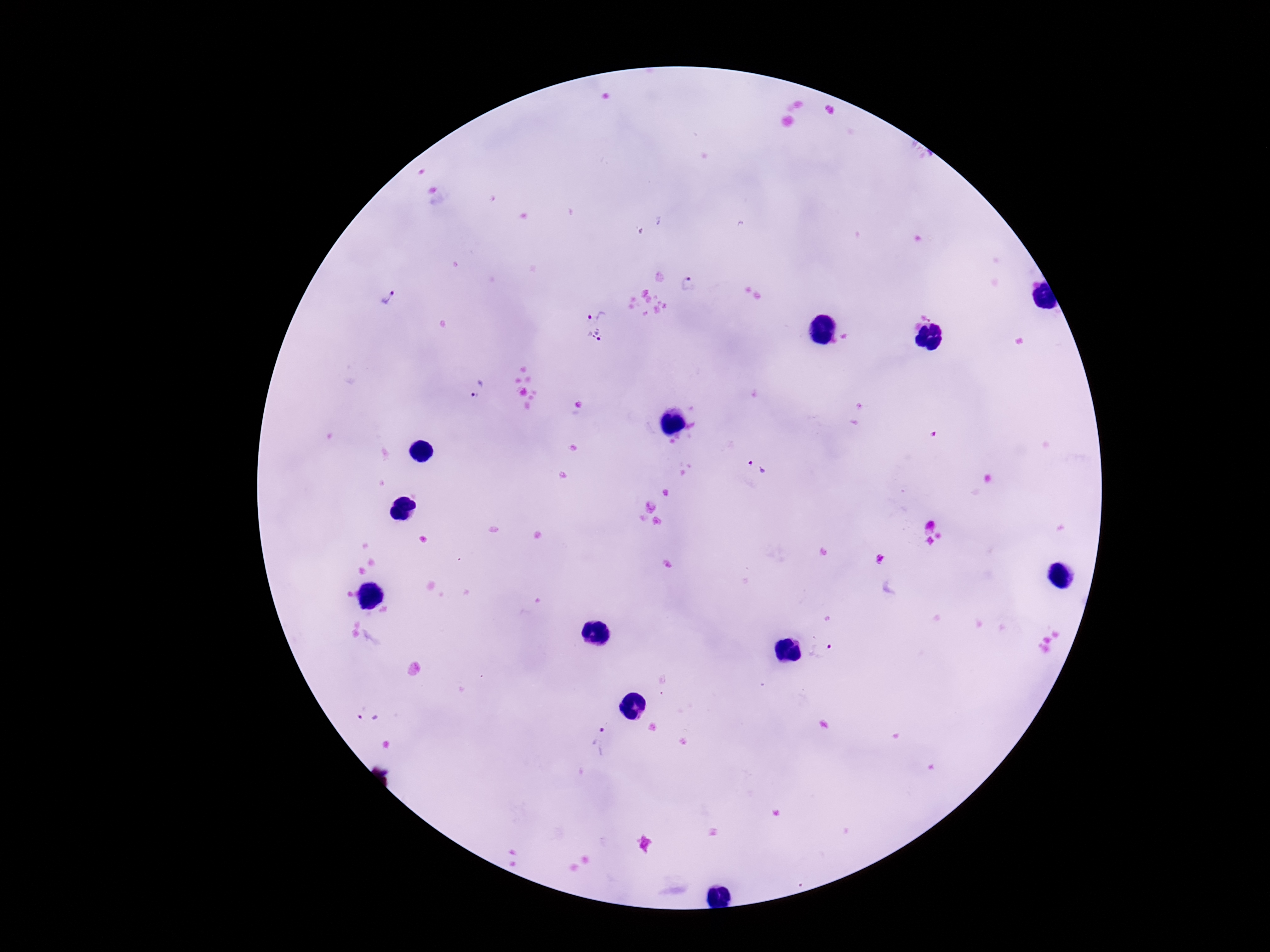
image size = 1270×952 pixels
Plasmodium parasite locations = approximate centers as (x, y) in pixels: (692, 284), (386, 299), (595, 308), (598, 342), (478, 389), (757, 468), (823, 650), (371, 711), (600, 740)
patient malaria status = infected
preparation = thick blood film
capture = smartphone camera through the microscope eyepiece
magnification = 100x
field of view = single
stain = Giemsa